Comment on the morphology of the erythrocytes.
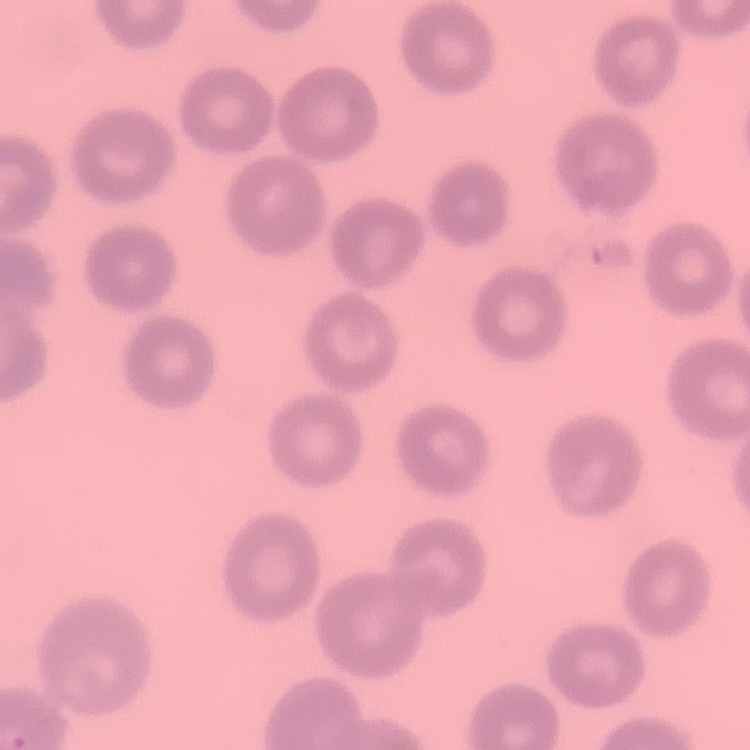

They show no rouleaux formation.

stain = Field's or Giemsa
image type = one tile cut from a larger photomicrograph
preparation = thin peripheral smear